Give the extent of all Plasmodium falciparum-infected red blood cells.
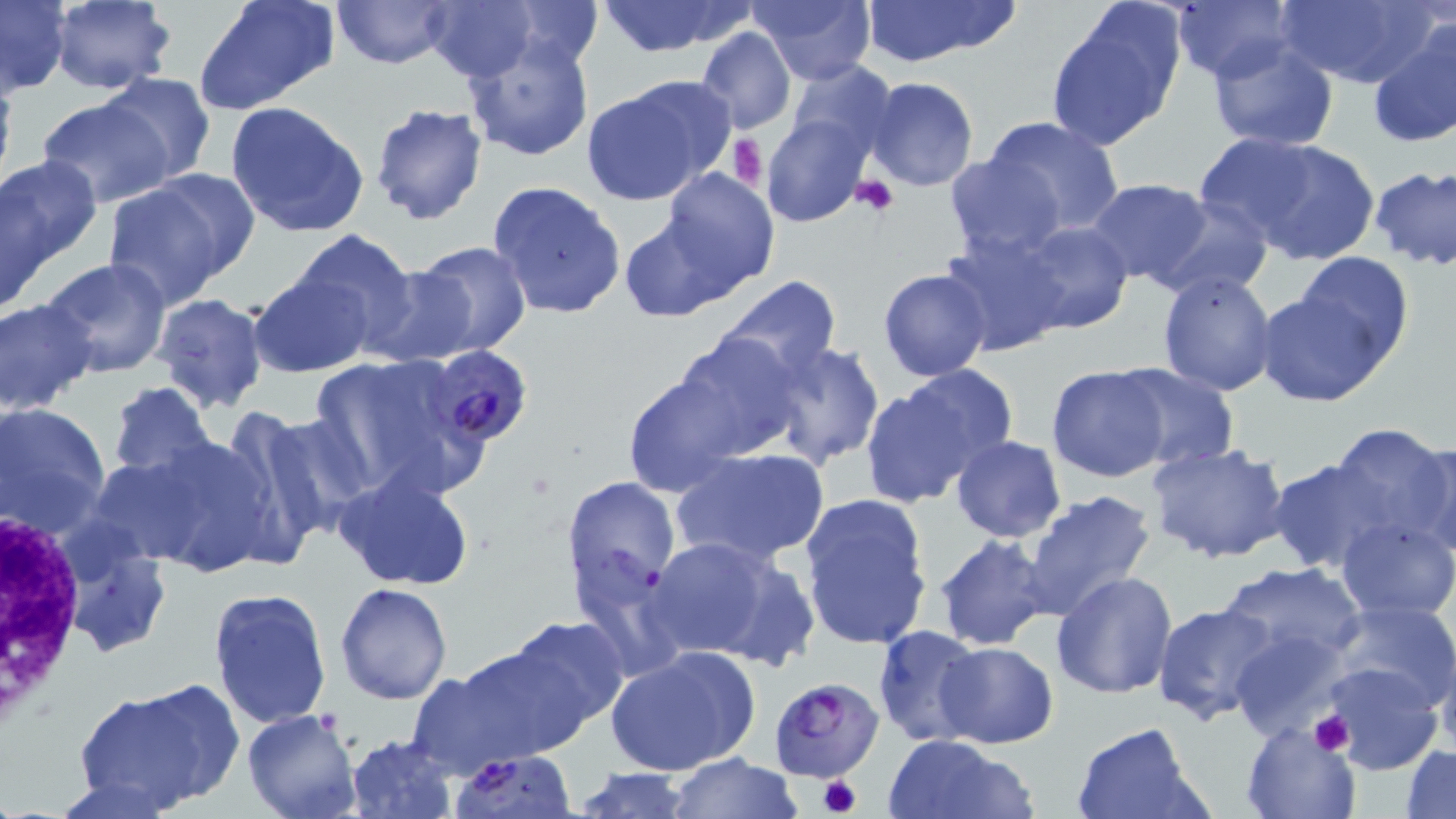

Approximate bounding boxes as (x1,y1)-(x2,y2) corner pairs in pixels.
Plasmodium falciparum-infected red blood cells: (426,345)-(534,446), (769,675)-(882,782).

Summary:
  - Uninfected red blood cell locations: (47,0)-(177,94), (332,0)-(453,70), (423,0)-(541,83), (502,0)-(603,67), (593,0)-(754,57), (857,0)-(1016,67), (194,1)-(340,115), (750,1)-(876,84), (1171,1)-(1296,84), (1275,1)-(1431,88), (1,2)-(70,94), (1046,5)-(1185,152), (1367,22)-(1456,149), (695,27)-(797,134), (464,32)-(595,163), (1205,34)-(1341,151), (783,60)-(895,164), (0,67)-(17,199), (99,73)-(218,185), (581,77)-(733,205), (863,77)-(979,191), (34,96)-(175,207), (225,100)-(370,238), (370,102)-(487,225), (980,115)-(1125,240), (763,117)-(870,228), (1194,132)-(1325,240), (1234,137)-(1381,264), (1,154)-(102,275), (944,155)-(1066,260), (1369,165)-(1456,269), (657,168)-(778,292), (101,176)-(248,308), (1083,178)-(1214,287), (2,180)-(58,314), (487,181)-(625,320), (1150,195)-(1274,300), (619,214)-(739,321), (1014,221)-(1133,336), (290,230)-(420,347), (937,231)-(1070,356), (408,240)-(534,359), (1288,250)-(1417,369), (40,256)-(173,380), (364,266)-(479,367), (879,268)-(993,381), (1157,271)-(1278,397), (251,272)-(371,378), (719,276)-(842,385), (1255,289)-(1393,408), (152,293)-(269,413), (0,298)-(98,417), (669,330)-(805,464), (764,340)-(885,471), (307,353)-(482,496), (1046,364)-(1173,482), (1109,364)-(1239,472), (860,370)-(1014,505), (619,371)-(747,497), (108,382)-(216,483), (1,402)-(110,533), (238,407)-(373,545), (1329,422)-(1452,553), (1418,432)-(1456,561), (126,434)-(279,577), (950,435)-(1067,543), (1147,440)-(1294,564), (674,448)-(828,566), (1267,457)-(1397,574), (334,470)-(478,592), (560,473)-(680,604), (1020,490)-(1158,621), (798,492)-(933,652), (1336,516)-(1455,618), (57,529)-(170,659), (932,533)-(1056,652), (645,535)-(807,665), (1217,562)-(1367,668), (1050,569)-(1180,700), (336,581)-(452,703), (208,587)-(332,730), (1328,600)-(1456,715), (1152,602)-(1283,726), (501,613)-(630,738), (870,626)-(986,746), (1229,630)-(1353,739), (1435,636)-(1456,758), (448,638)-(592,763), (935,642)-(1057,748), (607,644)-(760,778), (1323,663)-(1443,774), (408,670)-(514,776), (73,689)-(220,813), (242,709)-(361,819), (1241,721)-(1359,818), (1070,723)-(1211,819), (884,733)-(1035,819), (344,734)-(457,819), (1401,744)-(1456,818), (447,750)-(578,818), (666,753)-(802,819), (571,767)-(696,819)
  - Platelet locations: (729,133)-(765,194), (851,176)-(900,218), (1308,711)-(1355,758), (816,773)-(863,815)
  - White blood cell locations: (0,507)-(88,731)
  - Slide-level diagnosis: Plasmodium falciparum
  - Modality: optical microscopy
  - Preparation: thin blood film
  - Magnification: 1000x
  - Field of view: one of a larger specimen
  - Image size: 1456×819 pixels
  - Stain: May-Grünwald-Giemsa